Name the blood parasite species.
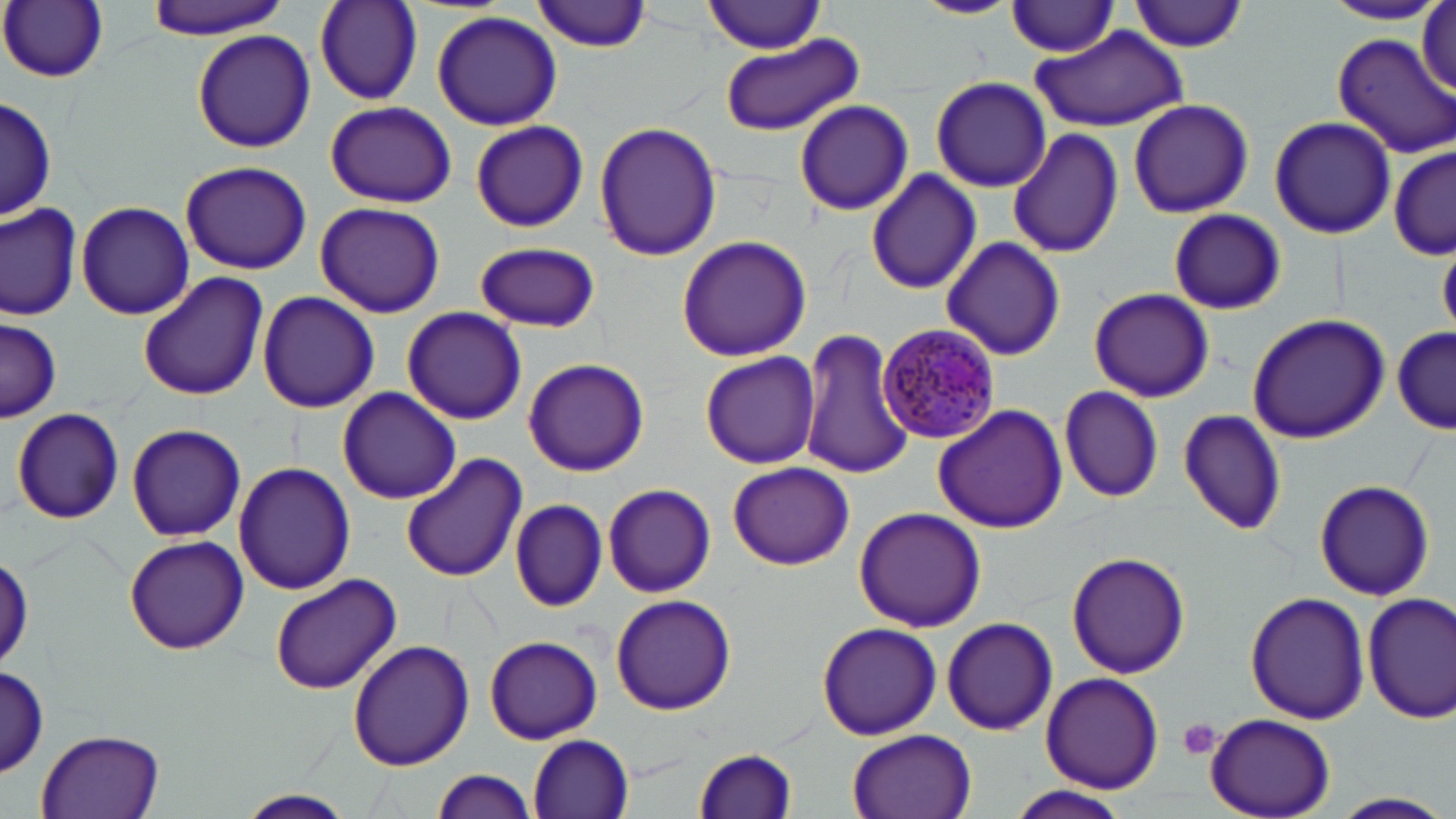

Plasmodium malariae.

Approximate bounding boxes as (x1,y1)-(x2,y2) corner pairs in pixels. Uninfected red blood cell locations: (141,0)-(290,38), (314,0)-(423,107), (535,0)-(653,51), (913,0)-(1020,19), (2,1)-(108,83), (703,1)-(830,54), (1130,1)-(1248,52), (1319,1)-(1445,26), (1005,3)-(1124,56), (1416,5)-(1454,96), (432,10)-(562,131), (191,28)-(316,155), (1031,29)-(1187,133), (720,33)-(863,138), (1331,33)-(1455,159), (929,76)-(1052,192), (1,96)-(55,225), (794,99)-(913,215), (944,100)-(1094,238), (1127,100)-(1253,218), (324,101)-(456,208), (1269,116)-(1396,240), (471,121)-(588,232), (593,121)-(722,263), (1009,128)-(1124,261), (1391,144)-(1456,259), (181,161)-(311,275), (865,170)-(981,295), (76,200)-(194,319), (314,201)-(445,318), (0,203)-(81,319), (1168,209)-(1285,315), (675,235)-(811,362), (940,237)-(1065,360), (475,240)-(600,333), (1439,240)-(1456,335), (138,272)-(268,400), (1088,287)-(1214,402), (258,290)-(379,414), (400,306)-(527,425), (1246,312)-(1391,444), (0,318)-(61,421), (799,325)-(915,481), (1392,326)-(1455,435), (700,351)-(820,468), (522,357)-(650,477), (1059,384)-(1164,502), (336,388)-(463,503), (932,404)-(1067,536), (11,408)-(124,523), (1176,408)-(1286,537), (126,425)-(246,542), (401,454)-(526,582), (234,461)-(357,595), (727,462)-(854,570), (1314,479)-(1435,602), (603,484)-(717,598), (510,498)-(607,612), (853,506)-(986,631), (123,535)-(249,653), (1,548)-(33,672), (1066,552)-(1191,680), (268,573)-(402,695), (1244,590)-(1370,725), (1361,592)-(1456,723), (609,594)-(737,716), (941,616)-(1059,736), (816,622)-(941,740), (484,634)-(602,745), (347,639)-(474,771), (0,666)-(49,775), (1039,672)-(1165,793), (1205,714)-(1335,818), (36,728)-(166,819), (848,730)-(974,819), (530,734)-(635,817), (692,748)-(799,819), (432,768)-(538,819), (1005,786)-(1132,819), (235,789)-(356,819), (1334,791)-(1451,817). Platelet locations: (1178,718)-(1223,763). Plasmodium malariae-infected red blood cell locations: (879,321)-(1000,442). May-Grünwald-Giemsa-stained preparation. Image is 1456×819 pixels. One field of a larger specimen. Thin blood film. Light microscopy. Captured at 1000x magnification.